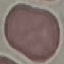

Summary:
  - Result: no malaria parasites seen
  - Capture: smartphone through the microscope eyepiece
  - Preparation: thin blood film
  - Image type: automatically extracted cell patch, resized to 64 × 64 pixels
  - Stain: Giemsa